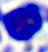
Summary:
  - Modality: photomicrograph
  - Identification: leukocyte
  - Magnification: 400x